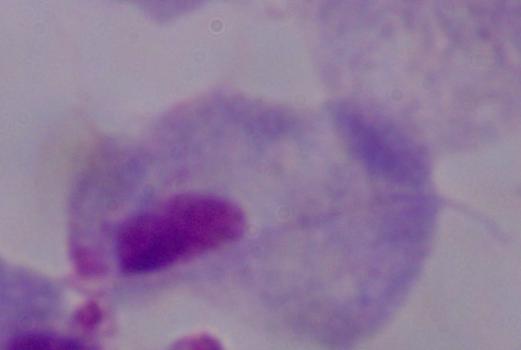
Photomicrograph. A trichomonad is seen. 1000x magnification.